Locate and identify every blood parasite.
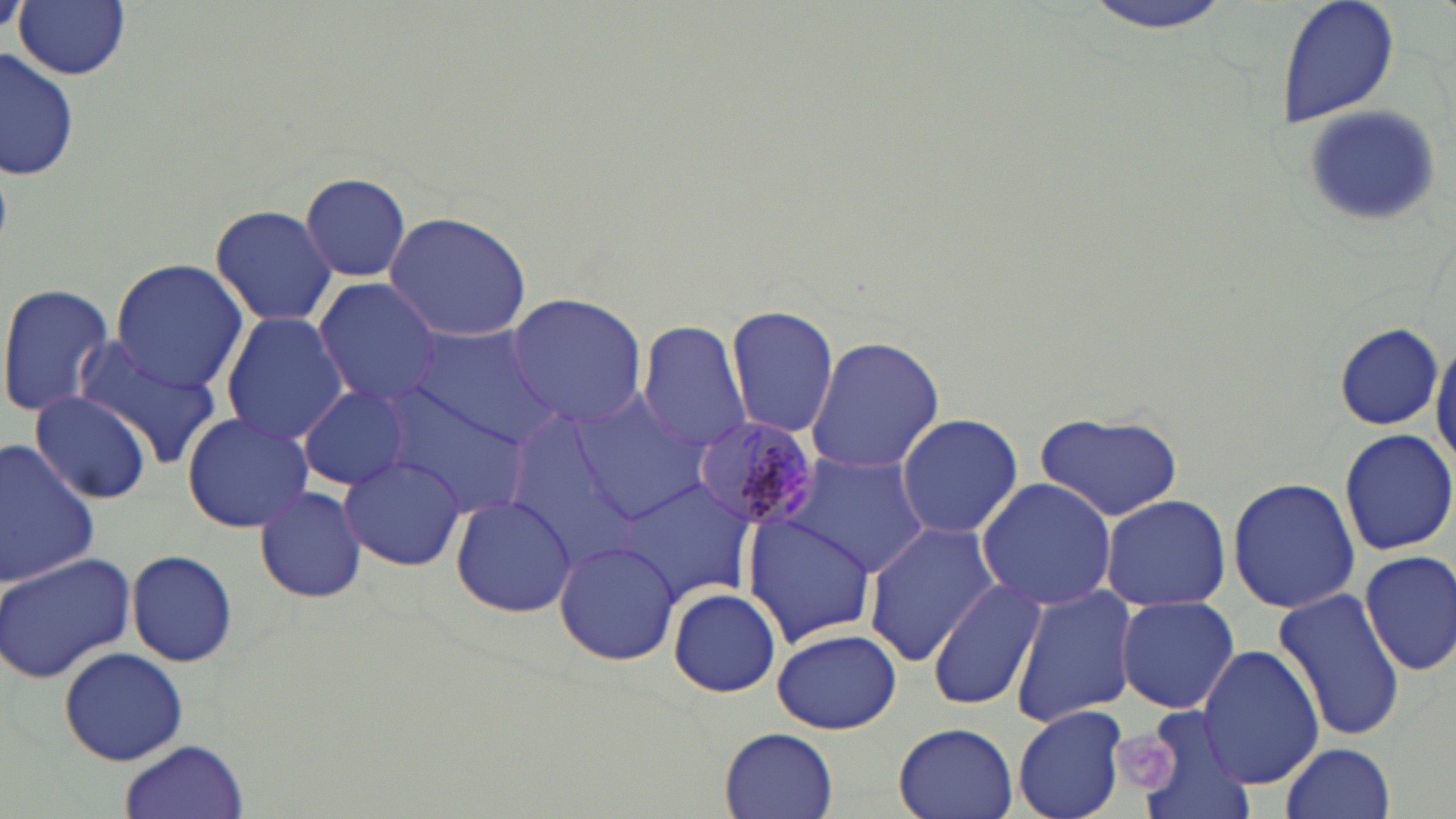
Approximate bounding boxes as [x1, y1, x2, y2] in pixels.
Plasmodium malariae-infected red blood cells: [691, 416, 823, 531].
No Plasmodium falciparum, Plasmodium ovale, Plasmodium vivax, Babesia divergens, or Trypanosoma brucei observed.

{
  "slide_level_diagnosis": "Plasmodium malariae",
  "magnification": "1000x",
  "stain": "May-Grünwald-Giemsa",
  "platelet_locations": "approximate bounding boxes as [x1, y1, x2, y2] in pixels: [1118, 728, 1185, 801]",
  "image_size": "1456×819 pixels",
  "field_of_view": "single",
  "preparation": "thin blood smear",
  "modality": "light microscopy",
  "uninfected_red_blood_cell_locations": "approximate bounding boxes as [x1, y1, x2, y2] in pixels: [14, 0, 131, 81], [1077, 0, 1236, 33], [1275, 0, 1399, 128], [1, 49, 82, 180], [1303, 101, 1448, 230], [298, 173, 410, 282], [210, 203, 338, 328], [383, 211, 533, 343], [111, 259, 248, 394], [314, 280, 446, 408], [0, 281, 119, 420], [504, 293, 649, 428], [727, 306, 839, 438], [219, 312, 348, 447], [638, 320, 754, 455], [408, 323, 559, 444], [1334, 323, 1442, 429], [1431, 331, 1456, 474], [803, 335, 946, 475], [72, 337, 225, 468], [298, 384, 413, 492], [374, 384, 536, 519], [564, 389, 711, 523], [29, 391, 155, 505], [181, 410, 314, 533], [1035, 411, 1184, 522], [896, 413, 1024, 538], [1338, 427, 1454, 555], [0, 440, 100, 587], [785, 449, 929, 577], [338, 451, 467, 573], [1226, 476, 1360, 615], [977, 477, 1118, 611], [618, 480, 757, 606], [254, 485, 369, 605], [451, 495, 580, 617], [1099, 495, 1230, 610], [743, 510, 879, 647], [862, 520, 999, 666], [555, 539, 680, 667], [1359, 548, 1456, 678], [0, 549, 134, 685], [127, 549, 237, 668], [928, 577, 1047, 712], [1010, 583, 1139, 726], [668, 586, 781, 698], [1273, 587, 1405, 744], [1116, 595, 1240, 715], [773, 628, 902, 735], [1197, 644, 1323, 790], [59, 646, 188, 766], [1011, 704, 1128, 819], [1127, 707, 1253, 819], [892, 722, 1019, 819], [720, 727, 840, 818], [118, 740, 250, 819], [1280, 742, 1396, 819]"
}